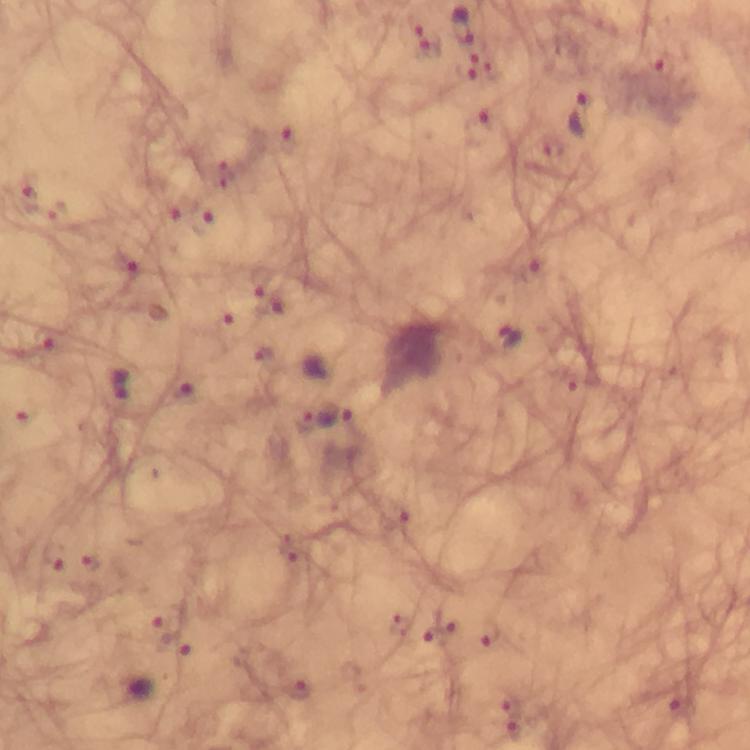 Approximate object centers, in pixels from the top-left corner. Plasmodium parasite locations: (x=461, y=26), (x=582, y=119), (x=29, y=197), (x=178, y=207), (x=206, y=224), (x=511, y=336), (x=45, y=340), (x=118, y=383), (x=185, y=392), (x=336, y=414), (x=51, y=557), (x=90, y=561), (x=161, y=627), (x=493, y=634), (x=434, y=638), (x=301, y=691), (x=509, y=703), (x=682, y=707), (x=515, y=730). Thick blood smear. From a diagnostic examination for malaria. Cropped region of a single field of view. Immersion oil applied. Smartphone photograph taken through a microscope. Image is 750×750 pixels. 100x magnification. Giemsa-stained preparation.